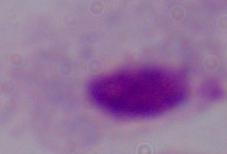

A trichomonad is shown. Captured at 1000x magnification. Micrograph.